Classify this cell by malaria status.
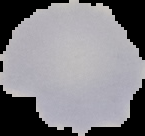
Uninfected.

Summary:
  - Preparation: thin blood film
  - Image size: 145×136 pixels
  - Image type: segmented cell region with the area outside set to black